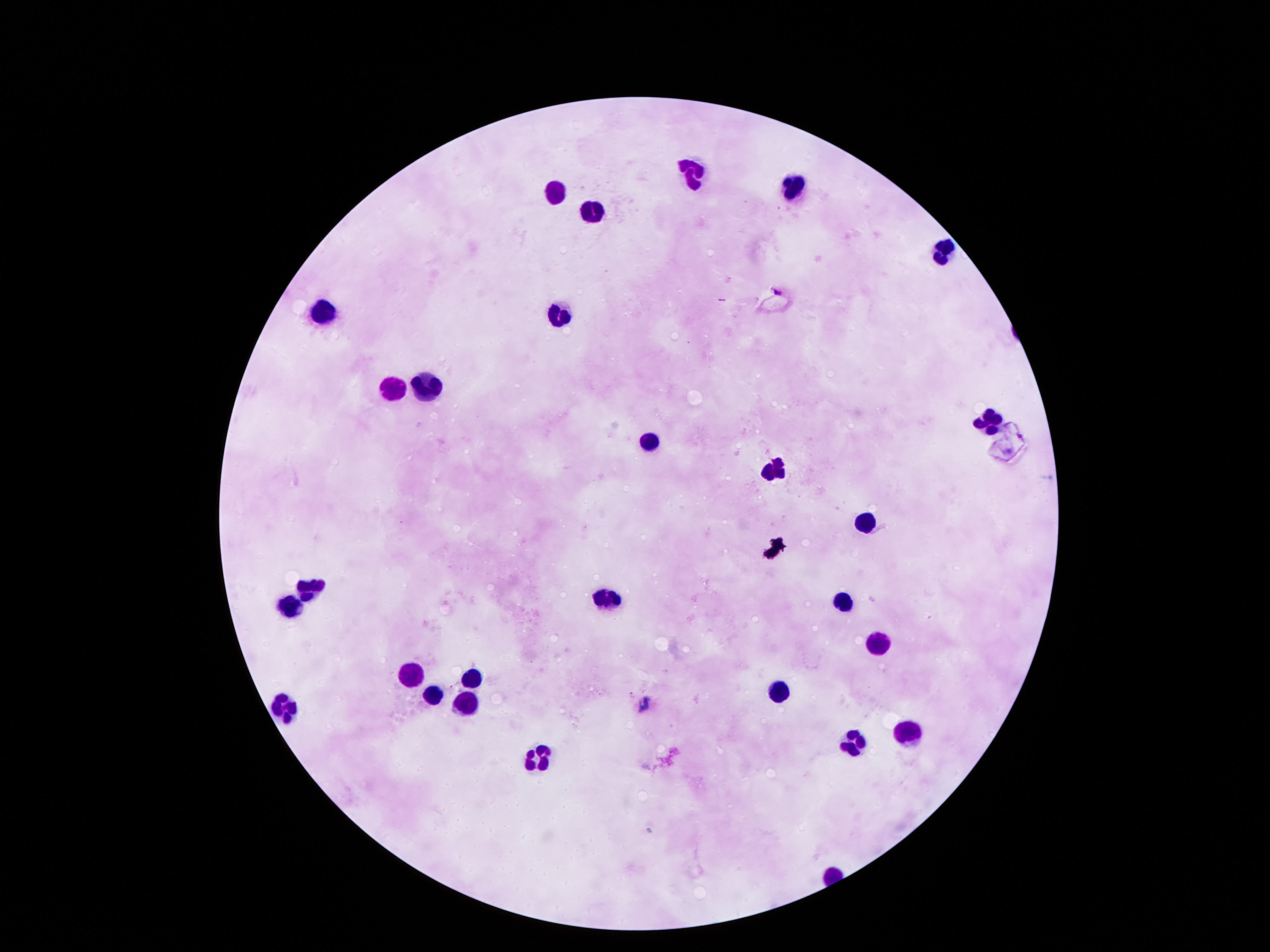
Approximate centers as {x, y} in pixels.
Summary:
  - Leukocyte locations: {691, 171}, {553, 189}, {797, 189}, {590, 211}, {941, 246}, {324, 309}, {557, 318}, {424, 386}, {393, 389}, {989, 419}, {650, 439}, {775, 467}, {870, 519}, {309, 586}, {607, 597}, {844, 600}, {292, 606}, {878, 642}, {410, 672}, {472, 677}, {434, 691}, {780, 694}, {464, 701}, {285, 707}, {908, 729}, {856, 739}, {538, 755}
  - Field of view: single
  - Stain: Giemsa
  - Capture: smartphone camera through the microscope eyepiece
  - Magnification: 100x
  - Image size: 1270×952 pixels
  - Patient malaria status: negative
  - Preparation: thick blood film